Assess this cell for malaria.
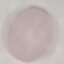
Uninfected.

Summary:
  - Stain: Giemsa
  - Preparation: thin smear
  - Image type: cell patch, automatically extracted from a larger field of view and resized to 64 × 64 pixels
  - Capture: smartphone through the microscope eyepiece